Comment on the morphology of the erythrocytes.
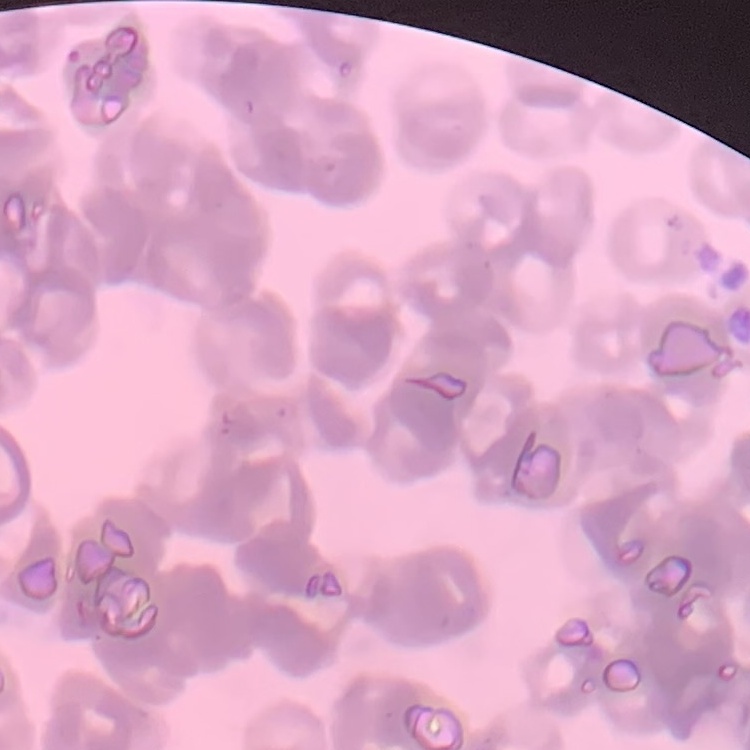

They show rouleaux formation.

image type = one tile cut from a larger photomicrograph
preparation = thin blood smear
stain = Field's or Giemsa